Locate and identify every blood parasite.
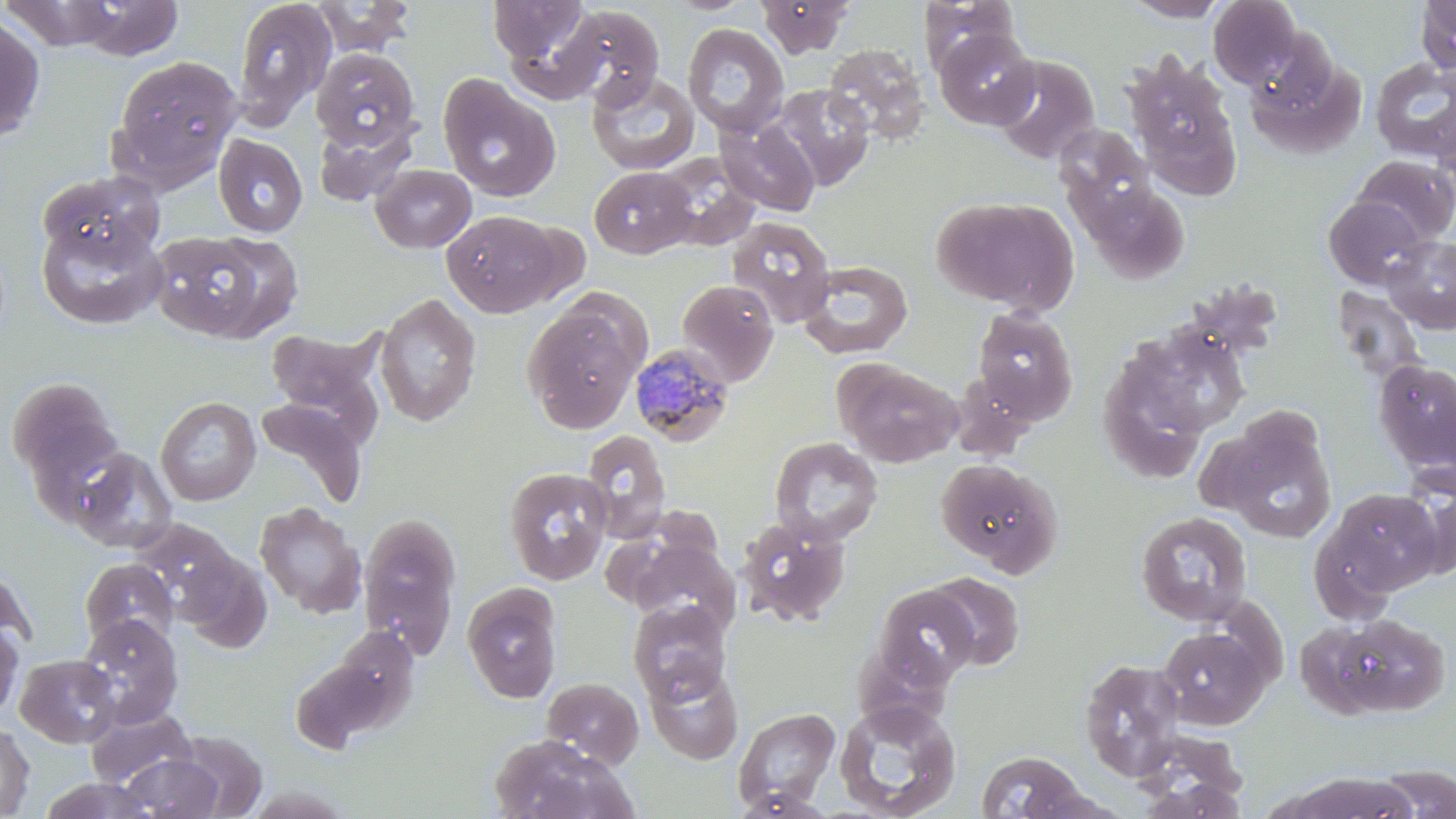

Approximate bounding boxes as (x1,y1)-(x2,y2) corner pairs in pixels.
Plasmodium malariae-infected red blood cells: (628,341)-(737,448).
No Plasmodium falciparum, Plasmodium ovale, Plasmodium vivax, Babesia divergens, or Trypanosoma brucei observed.

Uninfected red blood cell locations: (57,0)-(189,60), (312,0)-(417,56), (487,0)-(592,66), (664,0)-(755,16), (757,0)-(856,58), (1121,0)-(1230,22), (1208,0)-(1303,88), (1415,0)-(1456,73), (231,1)-(337,127), (917,1)-(1019,76), (559,6)-(666,108), (0,14)-(46,142), (682,23)-(790,138), (933,27)-(1039,129), (823,43)-(930,144), (1244,46)-(1367,159), (310,47)-(421,152), (1124,52)-(1239,186), (990,54)-(1101,165), (110,55)-(242,182), (1369,57)-(1456,161), (587,71)-(700,174), (439,76)-(560,201), (768,84)-(875,191), (1430,100)-(1456,196), (716,118)-(820,216), (1055,124)-(1159,226), (213,134)-(308,237), (653,153)-(760,249), (1351,154)-(1456,245), (370,164)-(477,253), (589,166)-(698,259), (37,170)-(164,268), (1081,181)-(1191,283), (932,195)-(1078,313), (1323,195)-(1430,290), (441,209)-(562,316), (725,216)-(837,328), (36,219)-(168,330), (149,230)-(276,341), (1382,235)-(1456,334), (798,260)-(914,358), (676,279)-(780,386), (1331,286)-(1427,386), (374,292)-(482,426), (522,303)-(644,433), (971,307)-(1079,424), (1132,324)-(1251,439), (265,326)-(388,440), (1097,350)-(1214,485), (1373,359)-(1456,474), (836,360)-(961,467), (6,377)-(123,497), (155,396)-(260,505), (255,398)-(368,509), (1220,420)-(1337,543), (581,429)-(670,542), (768,436)-(883,546), (67,446)-(177,553), (935,458)-(1062,574), (504,466)-(613,584), (1407,480)-(1456,582), (1325,488)-(1444,597), (254,502)-(366,618), (1134,511)-(1254,627), (357,513)-(463,660), (737,516)-(851,626), (126,519)-(241,619), (627,537)-(741,635), (176,551)-(273,654), (80,559)-(179,649), (0,564)-(35,658), (924,572)-(1025,670), (462,583)-(563,704), (872,584)-(980,691), (628,600)-(732,703), (1319,612)-(1452,719), (76,614)-(184,727), (0,620)-(23,720), (322,626)-(419,728), (1157,626)-(1270,729), (15,653)-(121,748), (291,654)-(398,750), (1078,658)-(1187,780), (645,662)-(744,764), (541,677)-(644,769), (834,699)-(962,819), (85,705)-(197,788), (733,707)-(841,811), (0,722)-(35,817), (173,731)-(268,817), (488,734)-(633,819), (974,750)-(1095,819), (118,754)-(223,818), (1374,766)-(1455,818), (1287,773)-(1419,818), (1134,774)-(1251,818), (39,776)-(159,819), (731,789)-(841,819). Slide-level diagnosis: Plasmodium malariae. One field of a larger specimen. May-Grünwald-Giemsa-stained preparation. Thin blood smear. Image is 1456×819 pixels. Light microscopy. Captured at 1000x magnification.